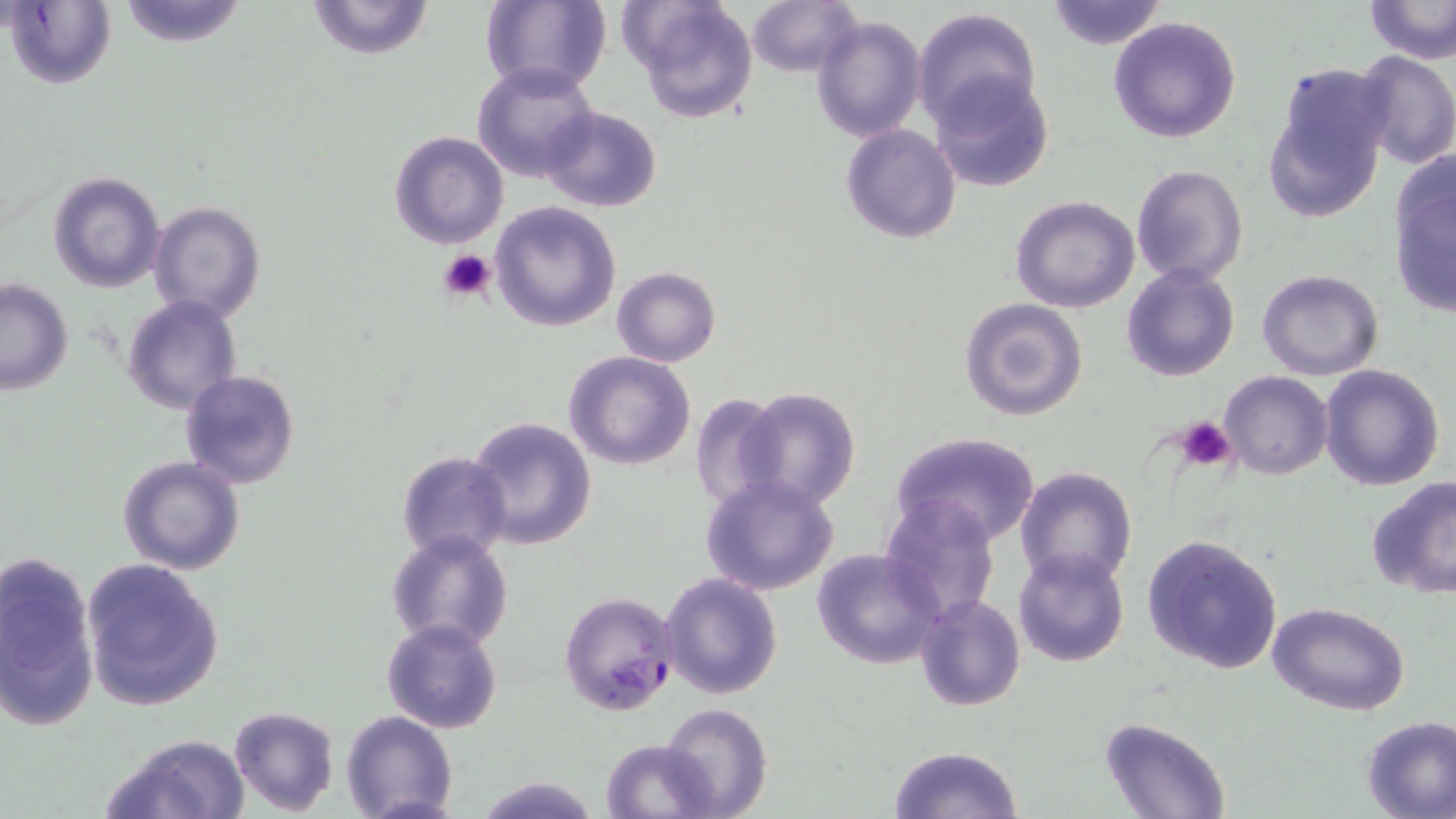
slide-level diagnosis = Plasmodium falciparum
magnification = 1000x
modality = optical microscopy
uninfected red blood cell locations = approximate bounding boxes as named x1/y1/x2/y2 corners in pixels: (x1=113, y1=0, x2=253, y2=47), (x1=302, y1=0, x2=437, y2=61), (x1=479, y1=0, x2=612, y2=96), (x1=622, y1=0, x2=761, y2=124), (x1=745, y1=0, x2=859, y2=78), (x1=1045, y1=0, x2=1167, y2=51), (x1=1363, y1=0, x2=1456, y2=64), (x1=5, y1=1, x2=117, y2=90), (x1=910, y1=6, x2=1042, y2=128), (x1=810, y1=13, x2=927, y2=142), (x1=1107, y1=15, x2=1243, y2=143), (x1=1351, y1=50, x2=1456, y2=169), (x1=473, y1=63, x2=600, y2=183), (x1=930, y1=72, x2=1054, y2=192), (x1=1263, y1=72, x2=1391, y2=223), (x1=540, y1=106, x2=661, y2=213), (x1=840, y1=124, x2=961, y2=244), (x1=388, y1=130, x2=509, y2=249), (x1=1387, y1=160, x2=1455, y2=318), (x1=1132, y1=164, x2=1249, y2=286), (x1=47, y1=171, x2=164, y2=293), (x1=1011, y1=196, x2=1140, y2=313), (x1=149, y1=200, x2=266, y2=323), (x1=489, y1=200, x2=623, y2=333), (x1=1121, y1=263, x2=1239, y2=382), (x1=611, y1=267, x2=720, y2=367), (x1=1257, y1=269, x2=1385, y2=380), (x1=0, y1=280, x2=73, y2=396), (x1=121, y1=296, x2=242, y2=415), (x1=959, y1=297, x2=1089, y2=422), (x1=563, y1=351, x2=696, y2=472), (x1=1317, y1=364, x2=1446, y2=490), (x1=178, y1=370, x2=301, y2=491), (x1=1219, y1=371, x2=1334, y2=479), (x1=735, y1=386, x2=862, y2=511), (x1=689, y1=391, x2=789, y2=519), (x1=466, y1=415, x2=597, y2=551), (x1=889, y1=431, x2=1041, y2=546), (x1=396, y1=451, x2=513, y2=564), (x1=117, y1=454, x2=245, y2=576), (x1=1014, y1=464, x2=1140, y2=589), (x1=700, y1=473, x2=840, y2=595), (x1=1365, y1=476, x2=1456, y2=601), (x1=879, y1=496, x2=1001, y2=623), (x1=385, y1=530, x2=514, y2=652), (x1=1141, y1=532, x2=1284, y2=674), (x1=812, y1=547, x2=946, y2=669), (x1=1013, y1=547, x2=1130, y2=669), (x1=0, y1=548, x2=99, y2=730), (x1=79, y1=557, x2=226, y2=710), (x1=660, y1=573, x2=783, y2=699), (x1=916, y1=592, x2=1025, y2=711), (x1=1266, y1=601, x2=1412, y2=716), (x1=382, y1=619, x2=503, y2=734), (x1=661, y1=702, x2=772, y2=819), (x1=228, y1=706, x2=340, y2=815), (x1=340, y1=711, x2=459, y2=819), (x1=1359, y1=715, x2=1456, y2=819), (x1=1099, y1=716, x2=1233, y2=819), (x1=99, y1=733, x2=250, y2=819), (x1=599, y1=738, x2=716, y2=819), (x1=887, y1=744, x2=1024, y2=819), (x1=473, y1=774, x2=600, y2=818)
platelet locations = approximate bounding boxes as named x1/y1/x2/y2 corners in pixels: (x1=438, y1=248, x2=498, y2=305), (x1=1177, y1=415, x2=1234, y2=470)
image size = 1456×819 pixels
Plasmodium falciparum-infected red blood cell locations = approximate bounding boxes as named x1/y1/x2/y2 corners in pixels: (x1=559, y1=589, x2=681, y2=718)
stain = May-Grünwald-Giemsa
field of view = one of a larger specimen
preparation = thin blood film